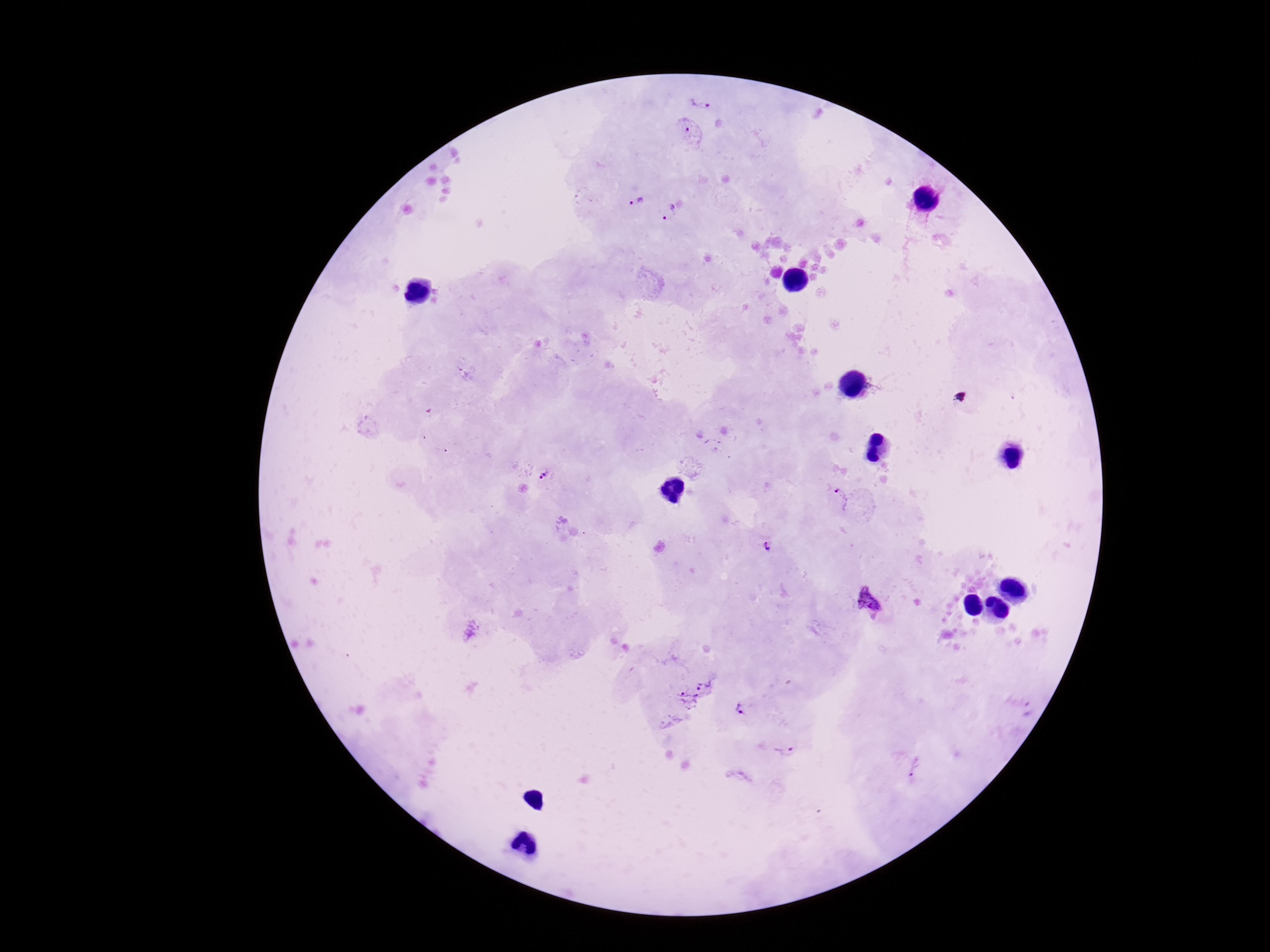

Approximate centers as [x, y] in pixels.
Summary:
  - Plasmodium parasite locations: [699, 106], [689, 133], [637, 201], [670, 213], [545, 479], [839, 499], [767, 546], [869, 601], [695, 689], [740, 709], [786, 752], [914, 767]
  - Preparation: thick blood smear
  - Capture: smartphone camera through the microscope eyepiece
  - Patient malaria status: positive
  - Field of view: single
  - Stain: Giemsa
  - Magnification: 100x
  - Image size: 1270×952 pixels